Locate and identify every blood parasite.
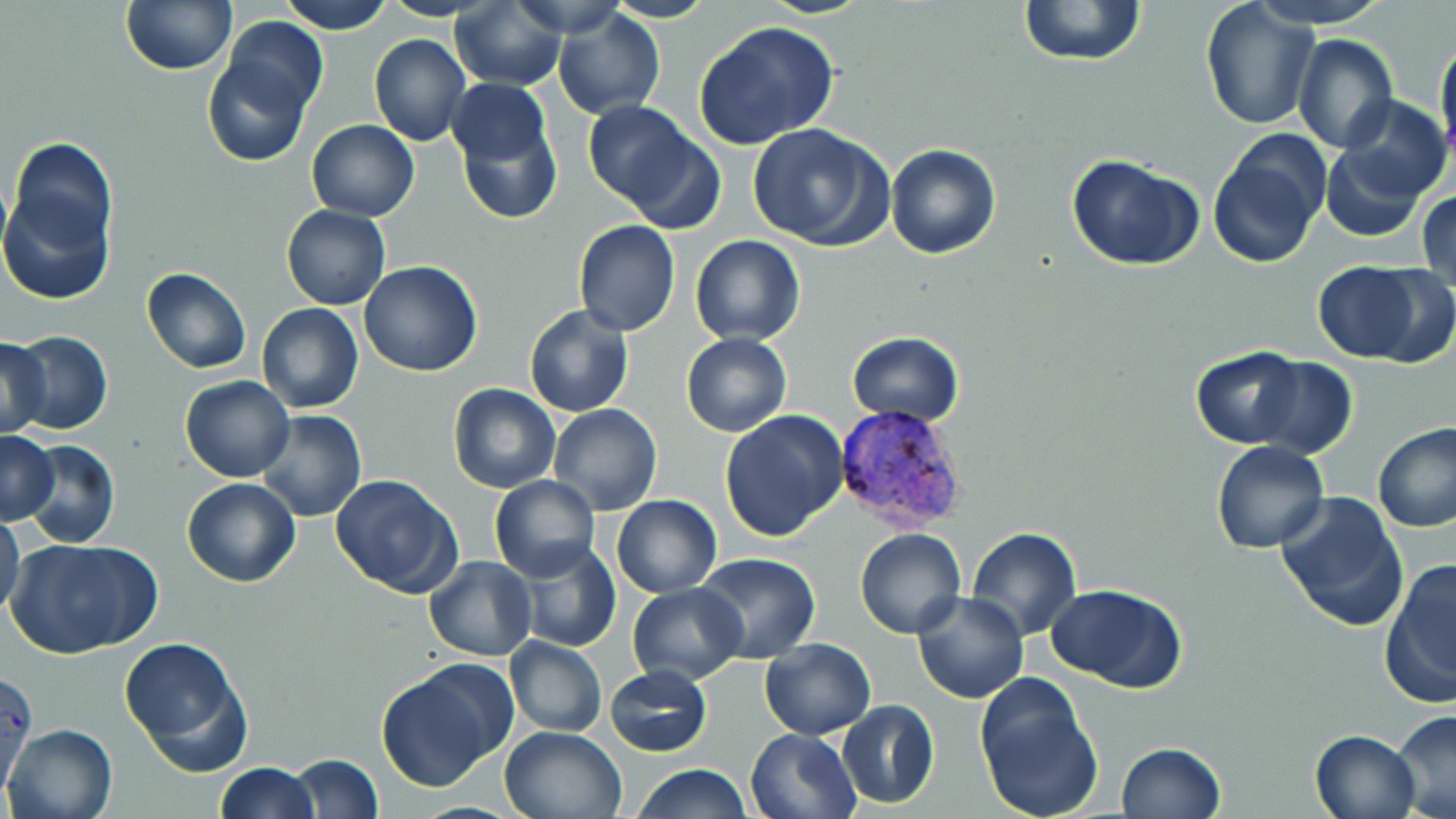
Approximate bounding boxes as named x1/y1/x2/y2 corners in pixels.
Plasmodium vivax-infected red blood cells: (x1=832, y1=401, x2=970, y2=535).
No Plasmodium falciparum, Plasmodium ovale, Plasmodium malariae, Babesia divergens, or Trypanosoma brucei observed.

Uninfected red blood cell locations: (x1=120, y1=0, x2=236, y2=76), (x1=277, y1=0, x2=396, y2=35), (x1=757, y1=0, x2=874, y2=19), (x1=1017, y1=0, x2=1147, y2=68), (x1=1248, y1=0, x2=1394, y2=28), (x1=605, y1=1, x2=716, y2=24), (x1=1199, y1=1, x2=1319, y2=131), (x1=451, y1=4, x2=567, y2=90), (x1=551, y1=8, x2=666, y2=120), (x1=221, y1=16, x2=329, y2=118), (x1=695, y1=20, x2=840, y2=149), (x1=369, y1=33, x2=472, y2=146), (x1=1292, y1=33, x2=1397, y2=153), (x1=1435, y1=35, x2=1456, y2=163), (x1=203, y1=54, x2=313, y2=167), (x1=448, y1=85, x2=561, y2=224), (x1=1334, y1=94, x2=1449, y2=204), (x1=582, y1=101, x2=714, y2=223), (x1=305, y1=119, x2=420, y2=220), (x1=746, y1=123, x2=892, y2=250), (x1=1206, y1=134, x2=1328, y2=269), (x1=9, y1=136, x2=117, y2=258), (x1=885, y1=143, x2=1000, y2=259), (x1=1320, y1=143, x2=1429, y2=241), (x1=1067, y1=154, x2=1205, y2=273), (x1=0, y1=176, x2=115, y2=307), (x1=1417, y1=188, x2=1455, y2=295), (x1=280, y1=204, x2=390, y2=309), (x1=574, y1=220, x2=680, y2=336), (x1=690, y1=235, x2=806, y2=346), (x1=358, y1=259, x2=483, y2=378), (x1=1311, y1=263, x2=1426, y2=363), (x1=1362, y1=265, x2=1456, y2=369), (x1=141, y1=268, x2=253, y2=374), (x1=256, y1=302, x2=364, y2=415), (x1=523, y1=304, x2=634, y2=418), (x1=9, y1=330, x2=114, y2=434), (x1=846, y1=330, x2=964, y2=427), (x1=681, y1=333, x2=791, y2=437), (x1=0, y1=335, x2=51, y2=438), (x1=1190, y1=347, x2=1309, y2=448), (x1=1247, y1=355, x2=1358, y2=459), (x1=180, y1=374, x2=294, y2=482), (x1=447, y1=383, x2=559, y2=493), (x1=547, y1=404, x2=664, y2=516), (x1=720, y1=409, x2=849, y2=542), (x1=255, y1=410, x2=367, y2=523), (x1=1372, y1=422, x2=1456, y2=533), (x1=1, y1=431, x2=58, y2=523), (x1=299, y1=431, x2=424, y2=560), (x1=21, y1=439, x2=120, y2=549), (x1=1211, y1=441, x2=1330, y2=554), (x1=330, y1=474, x2=461, y2=595), (x1=489, y1=476, x2=599, y2=583), (x1=182, y1=478, x2=301, y2=587), (x1=1274, y1=492, x2=1407, y2=632), (x1=611, y1=495, x2=721, y2=596), (x1=0, y1=513, x2=25, y2=623), (x1=967, y1=527, x2=1082, y2=642), (x1=856, y1=529, x2=966, y2=639), (x1=9, y1=539, x2=157, y2=658), (x1=511, y1=540, x2=621, y2=653), (x1=693, y1=552, x2=820, y2=664), (x1=425, y1=556, x2=537, y2=660), (x1=1379, y1=560, x2=1455, y2=710), (x1=627, y1=581, x2=747, y2=685), (x1=1046, y1=584, x2=1187, y2=694), (x1=911, y1=591, x2=1029, y2=705), (x1=119, y1=637, x2=254, y2=775), (x1=505, y1=637, x2=607, y2=737), (x1=759, y1=638, x2=875, y2=739), (x1=376, y1=661, x2=514, y2=791), (x1=605, y1=665, x2=711, y2=757), (x1=1, y1=671, x2=37, y2=797), (x1=973, y1=675, x2=1103, y2=819), (x1=836, y1=699, x2=940, y2=811), (x1=1391, y1=709, x2=1456, y2=819), (x1=3, y1=722, x2=117, y2=819), (x1=499, y1=726, x2=626, y2=819), (x1=746, y1=727, x2=862, y2=819), (x1=1310, y1=728, x2=1421, y2=819), (x1=1115, y1=741, x2=1225, y2=819), (x1=287, y1=753, x2=384, y2=818), (x1=215, y1=762, x2=319, y2=819), (x1=632, y1=765, x2=754, y2=819). Slide-level diagnosis: Plasmodium vivax. Captured at 1000x magnification. Image is 1456×819 pixels. Optical microscopy. Thin blood smear. Single field of view. May-Grünwald-Giemsa-stained preparation.